Name the parasite shown.
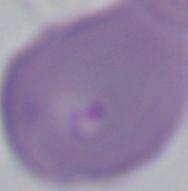

Babesia.

1000x magnification. Photomicrograph.